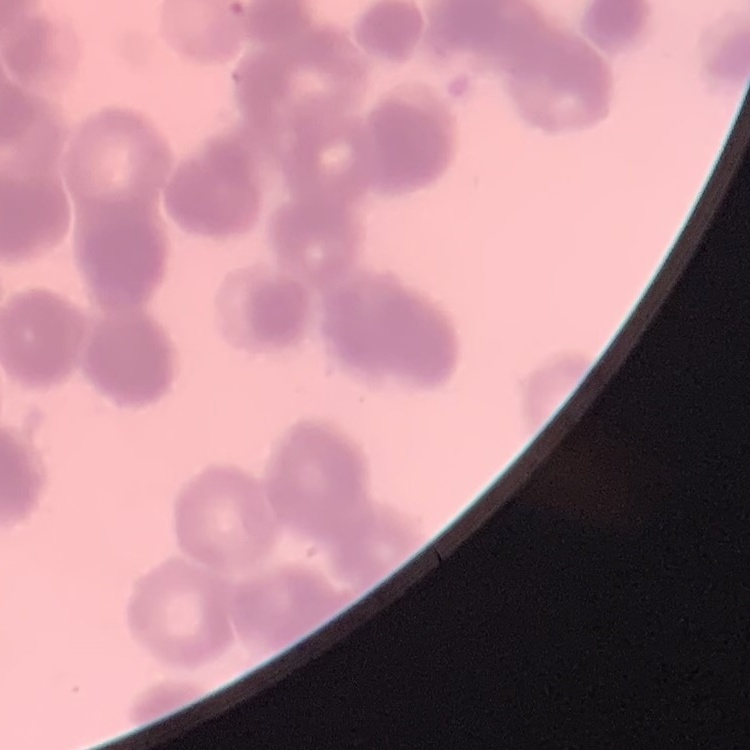

Summary:
  - Red blood cell morphology: rouleaux formation
  - Preparation: thin peripheral smear
  - Image type: one tile cut from a larger photomicrograph
  - Stain: Field's or Giemsa